Assess this cell for malaria.
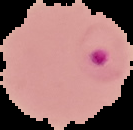
Parasitized.

Summary:
  - Image type: segmented cell region on a black background
  - Image size: 133×130 pixels
  - Preparation: thin blood film